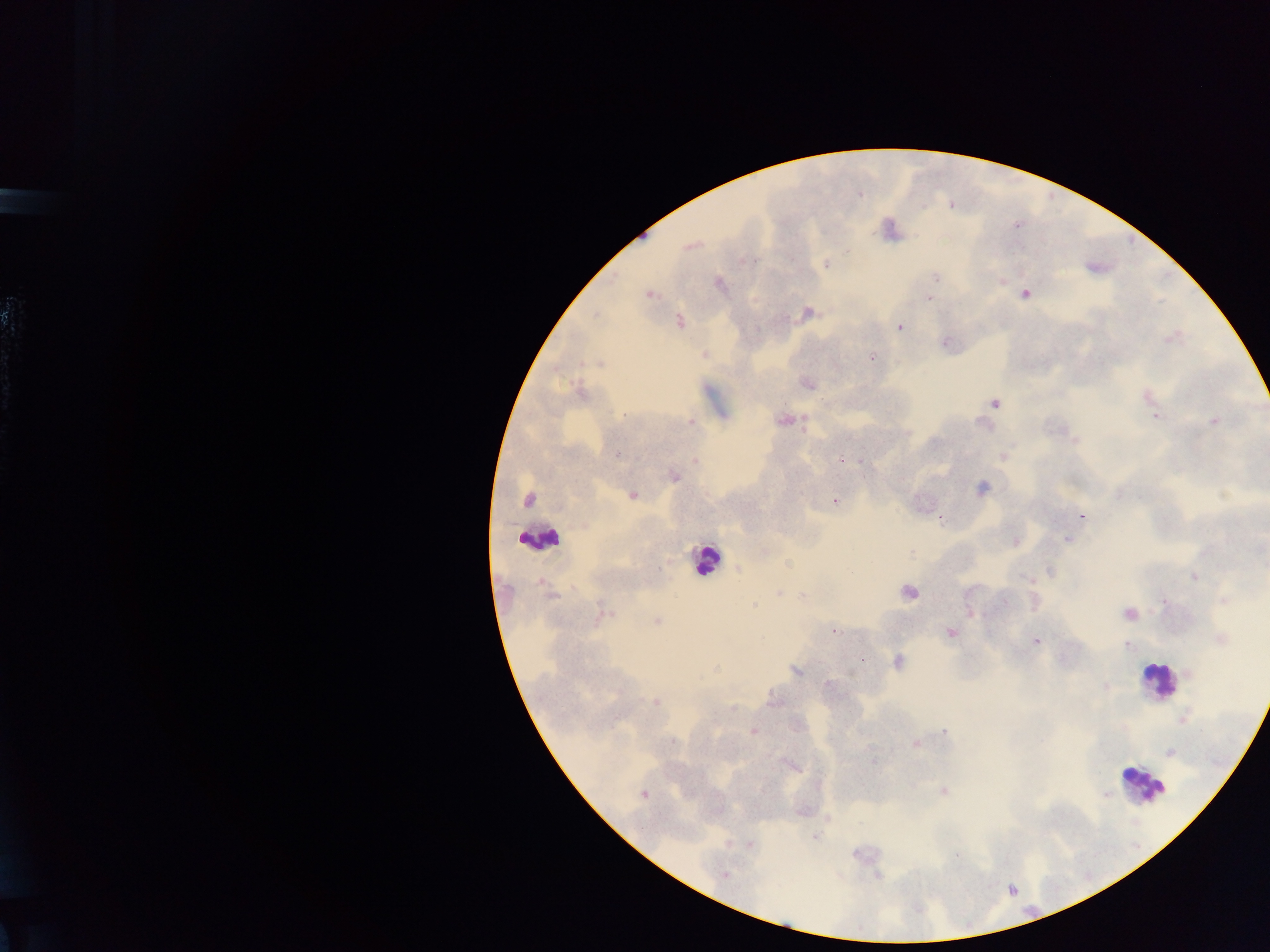

image_size: 1270×952 pixels
leukocyte_locations: 'approximate centers as [x, y] in pixels: [538, 539], [705, 560], [1158, 680], [1142, 785]'
country: Ghana
field_of_view: single
capture: mobile-phone photograph through a microscope
malaria_parasite_locations: 'approximate centers as [x, y] in pixels: [888, 229], [692, 245], [826, 264], [936, 278], [1001, 280], [718, 283], [649, 294], [1025, 294], [928, 297], [806, 313], [679, 320], [899, 327], [1171, 338], [947, 343], [704, 354], [872, 356], [807, 383], [579, 391], [1146, 396], [994, 403], [1155, 417], [784, 420], [1214, 421], [691, 422], [804, 426], [1075, 440], [617, 454], [1003, 455], [841, 457], [694, 461], [673, 476], [981, 488], [631, 495], [528, 498], [835, 501], [1081, 517], [1067, 538], [1015, 541], [765, 551], [1050, 571], [1194, 576], [541, 581], [908, 592], [778, 593], [802, 596], [1163, 600], [1226, 600], [754, 605], [970, 612], [1129, 613], [601, 615], [657, 621], [833, 630], [950, 632], [1220, 639], [1035, 641], [897, 662], [795, 671], [1105, 687], [655, 702], [1182, 718], [752, 731], [945, 732], [915, 742], [1169, 752], [942, 790], [643, 794], [1106, 794], [827, 820], [814, 836], [749, 844], [724, 875]'
preparation: thick blood film